Point out each Plasmodium parasite.
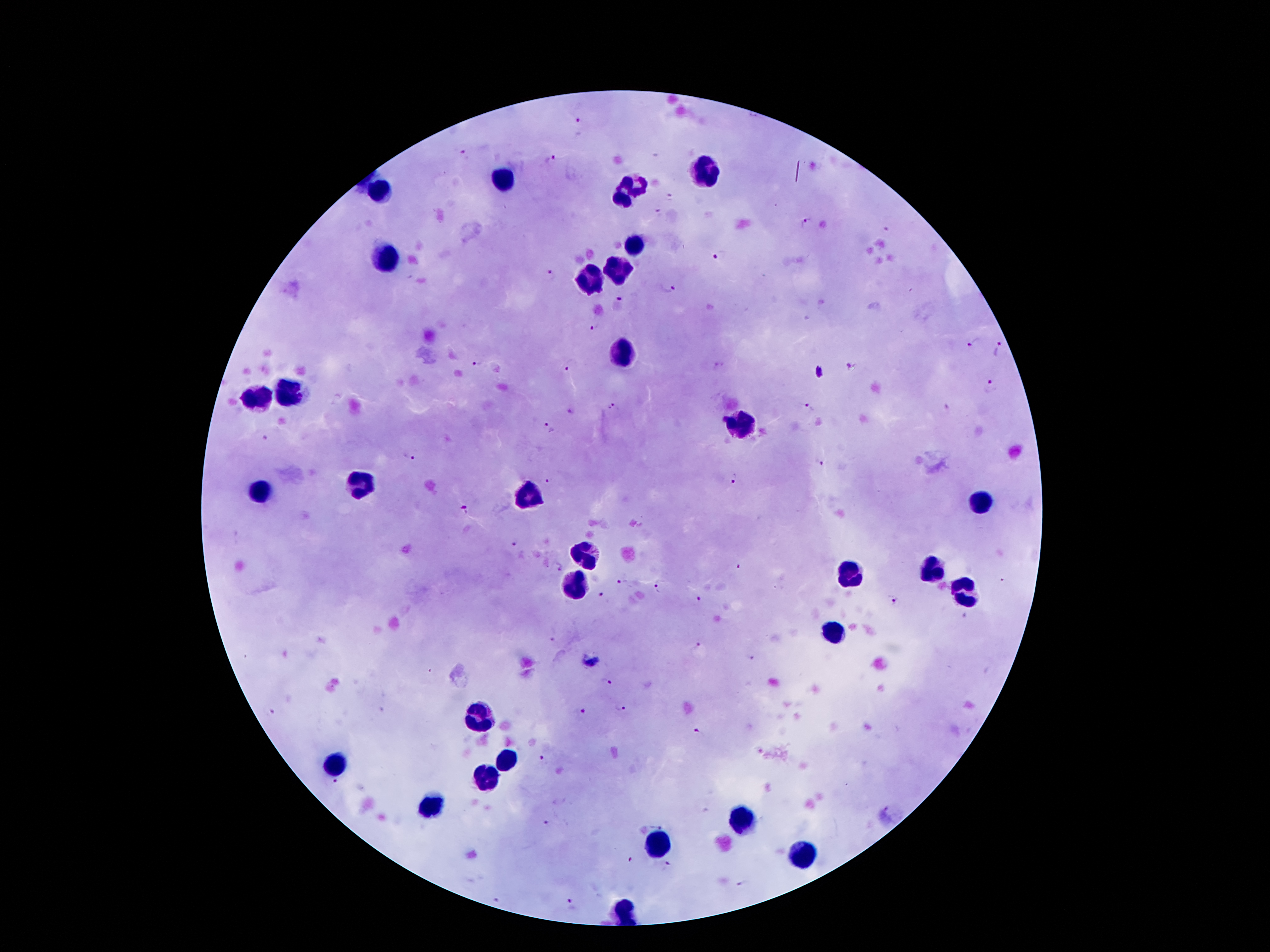
Approximate centers as {x, y} in pixels.
Plasmodium parasites: {579, 121}, {465, 155}, {549, 160}, {675, 195}, {660, 212}, {807, 224}, {885, 229}, {719, 255}, {551, 276}, {667, 289}, {620, 303}, {594, 325}, {973, 344}, {999, 351}, {572, 361}, {476, 363}, {853, 365}, {991, 386}, {613, 407}, {808, 409}, {571, 412}, {548, 429}, {265, 437}, {409, 457}, {821, 464}, {738, 478}, {550, 480}, {465, 510}, {513, 545}, {558, 567}, {739, 567}, {1003, 582}, {621, 583}, {661, 586}, {601, 595}, {700, 601}, {893, 601}, {552, 640}, {700, 648}, {749, 657}, {606, 680}, {621, 705}, {271, 712}, {584, 712}, {698, 735}, {543, 761}, {336, 785}, {657, 821}, {548, 823}, {629, 860}, {667, 864}, {744, 884}, {499, 900}, {573, 903}.

Leukocyte locations: {707, 172}, {505, 179}, {636, 182}, {383, 189}, {622, 200}, {630, 246}, {386, 258}, {617, 266}, {589, 279}, {623, 353}, {287, 391}, {257, 401}, {738, 424}, {360, 485}, {259, 492}, {529, 494}, {981, 503}, {584, 554}, {931, 568}, {852, 575}, {574, 586}, {964, 591}, {831, 637}, {480, 716}, {508, 760}, {335, 764}, {488, 777}, {430, 808}, {739, 822}, {658, 846}, {799, 854}, {624, 911}. Thick blood film. 100x magnification. Single field of view. Giemsa stain. Image is 1270×952 pixels. Patient malaria status: positive for Plasmodium falciparum. Smartphone photograph taken through the microscope eyepiece.